Draw a bounding box around every Plasmodium parasite, every leukocyte, and every artifact (stain precipitate or debris).
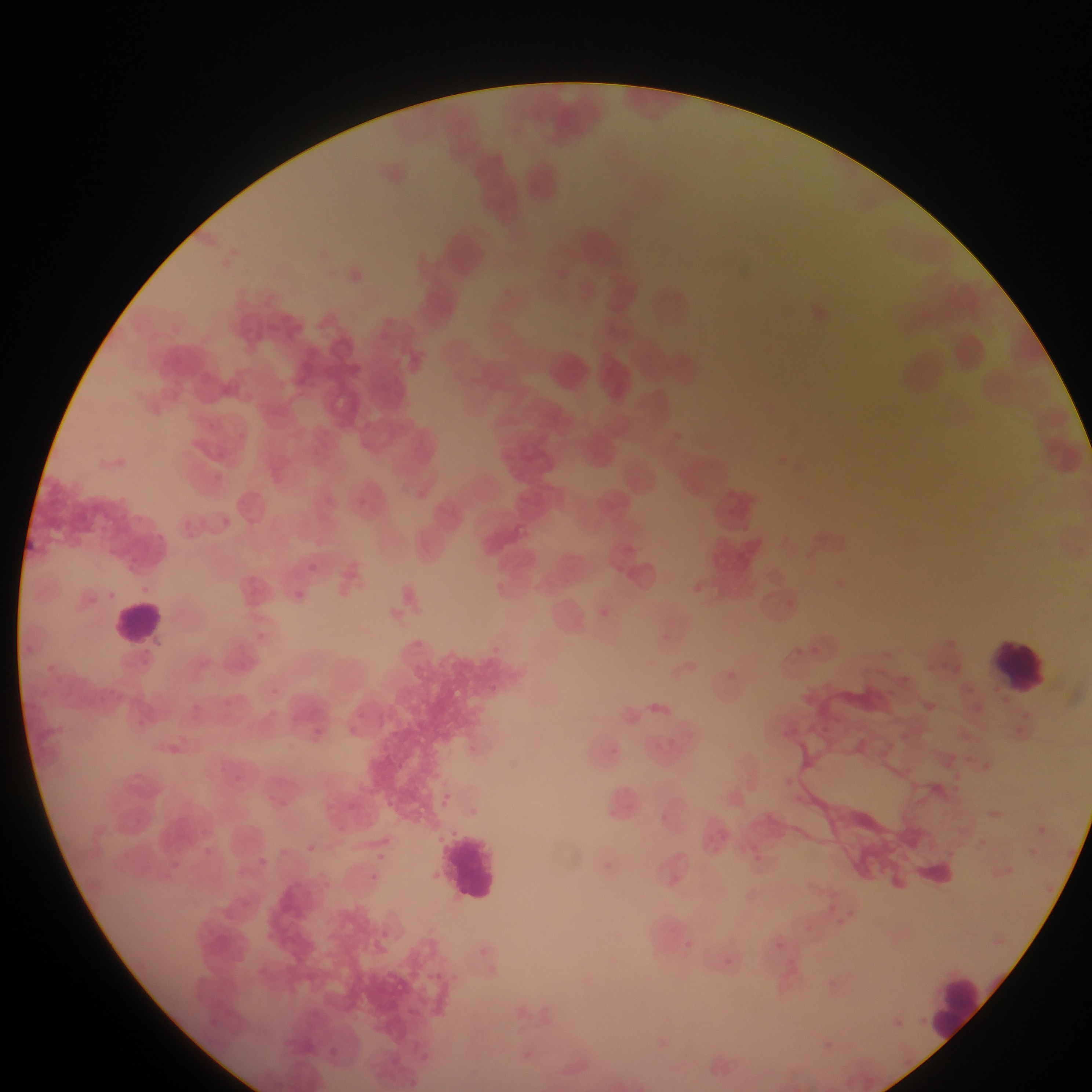
Approximate bounding boxes as {left, top, right, bottom} in pixels.
Plasmodium parasites: {356, 497, 365, 505}, {221, 517, 230, 527}, {245, 517, 254, 526}, {307, 563, 317, 572}, {295, 591, 305, 600}.
Leukocytes: {111, 599, 166, 647}, {992, 636, 1053, 695}, {442, 826, 506, 905}, {933, 974, 990, 1047}.

Summary:
  - Field of view: single
  - Capture: mobile-phone photograph through a microscope
  - Country: Ghana
  - Preparation: thin blood smear
  - Image size: 1092×1092 pixels